Locate every Plasmodium falciparum-infected red blood cell.
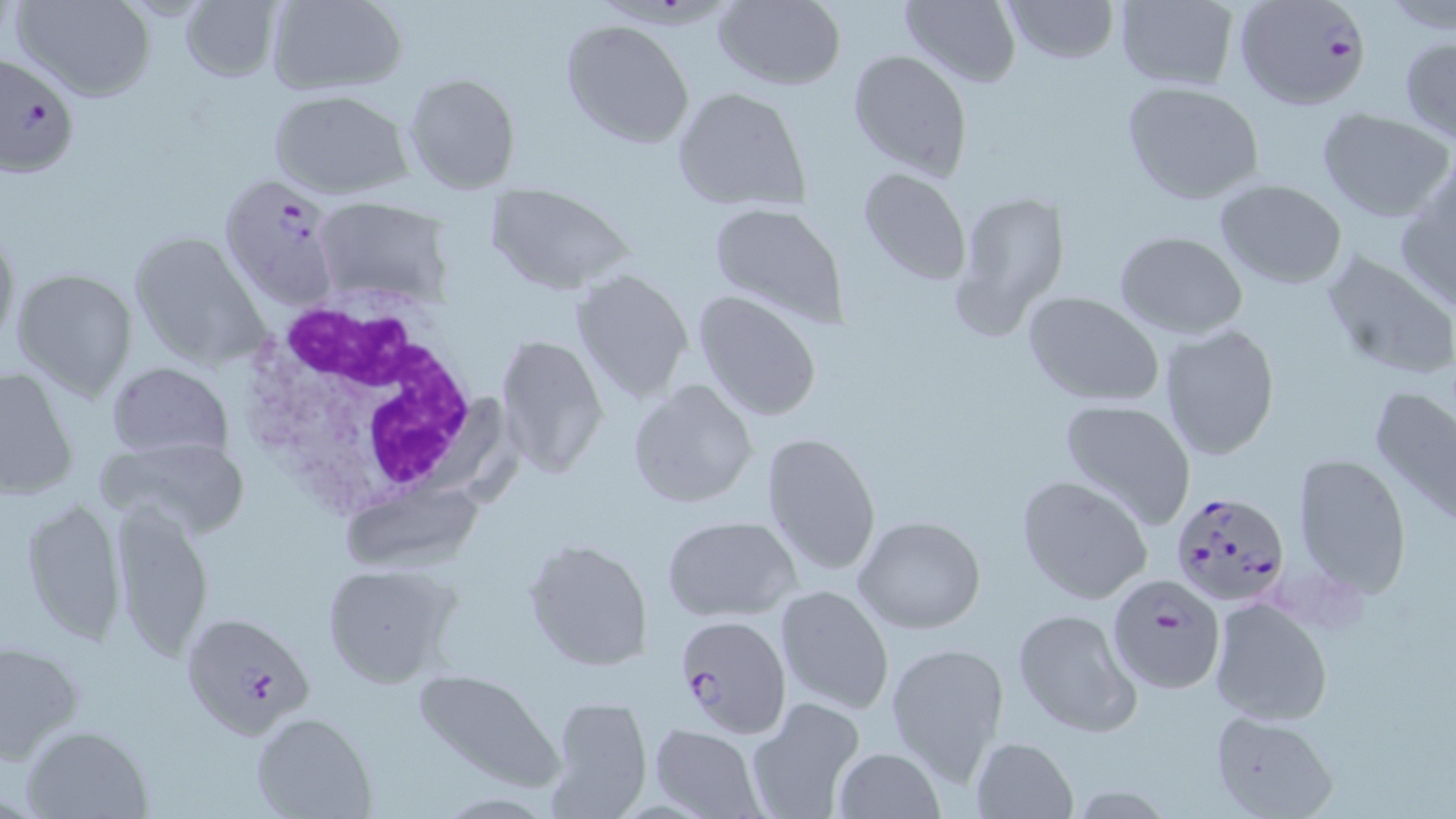
Approximate bounding boxes as [x1, y1, x2, y2] in pixels.
Plasmodium falciparum-infected red blood cells: [1234, 0, 1371, 114], [0, 51, 79, 183], [215, 175, 347, 310], [1171, 490, 1290, 609], [1106, 573, 1226, 693], [183, 610, 315, 739], [676, 613, 790, 737].

slide-level diagnosis = Plasmodium falciparum
stain = May-Grünwald-Giemsa
preparation = thin blood smear
uninfected red blood cell locations = approximate bounding boxes as [x1, y1, x2, y2] in pixels: [15, 0, 157, 102], [263, 0, 408, 96], [711, 0, 846, 90], [1002, 0, 1120, 66], [179, 1, 281, 82], [900, 1, 1021, 86], [1113, 1, 1240, 89], [558, 18, 698, 149], [1399, 34, 1456, 142], [847, 47, 974, 180], [403, 71, 521, 193], [1120, 81, 1263, 205], [671, 86, 812, 214], [270, 90, 411, 200], [1317, 108, 1454, 222], [856, 164, 974, 287], [1395, 175, 1456, 312], [1215, 180, 1349, 289], [485, 182, 634, 296], [949, 188, 1071, 341], [312, 199, 452, 307], [706, 200, 849, 327], [0, 223, 20, 351], [128, 231, 267, 367], [1115, 232, 1248, 339], [1319, 249, 1456, 381], [9, 268, 139, 401], [572, 269, 694, 403], [1021, 290, 1165, 406], [692, 291, 822, 422], [1158, 323, 1281, 460], [496, 334, 608, 478], [106, 361, 232, 460], [2, 366, 79, 502], [626, 379, 758, 510], [1370, 382, 1456, 527], [1058, 398, 1198, 529], [760, 431, 881, 576], [97, 436, 252, 542], [1292, 451, 1412, 596], [1016, 475, 1153, 607], [338, 480, 488, 575], [19, 493, 128, 648], [110, 498, 216, 662], [661, 514, 801, 621], [852, 515, 988, 636], [523, 536, 655, 672], [322, 561, 459, 689], [775, 584, 894, 715], [1207, 594, 1333, 726], [1012, 607, 1141, 736], [0, 638, 87, 761], [884, 639, 1011, 781], [411, 669, 565, 790], [544, 695, 654, 817], [746, 697, 866, 819], [251, 712, 375, 818], [1211, 712, 1338, 819], [22, 724, 151, 817], [650, 724, 765, 817], [970, 736, 1079, 819], [832, 747, 945, 819]
white blood cell locations = approximate bounding boxes as [x1, y1, x2, y2] in pixels: [236, 290, 488, 517]
magnification = 1000x
field of view = one of a larger specimen
modality = optical microscopy
image size = 1456×819 pixels